Classify the preparation.
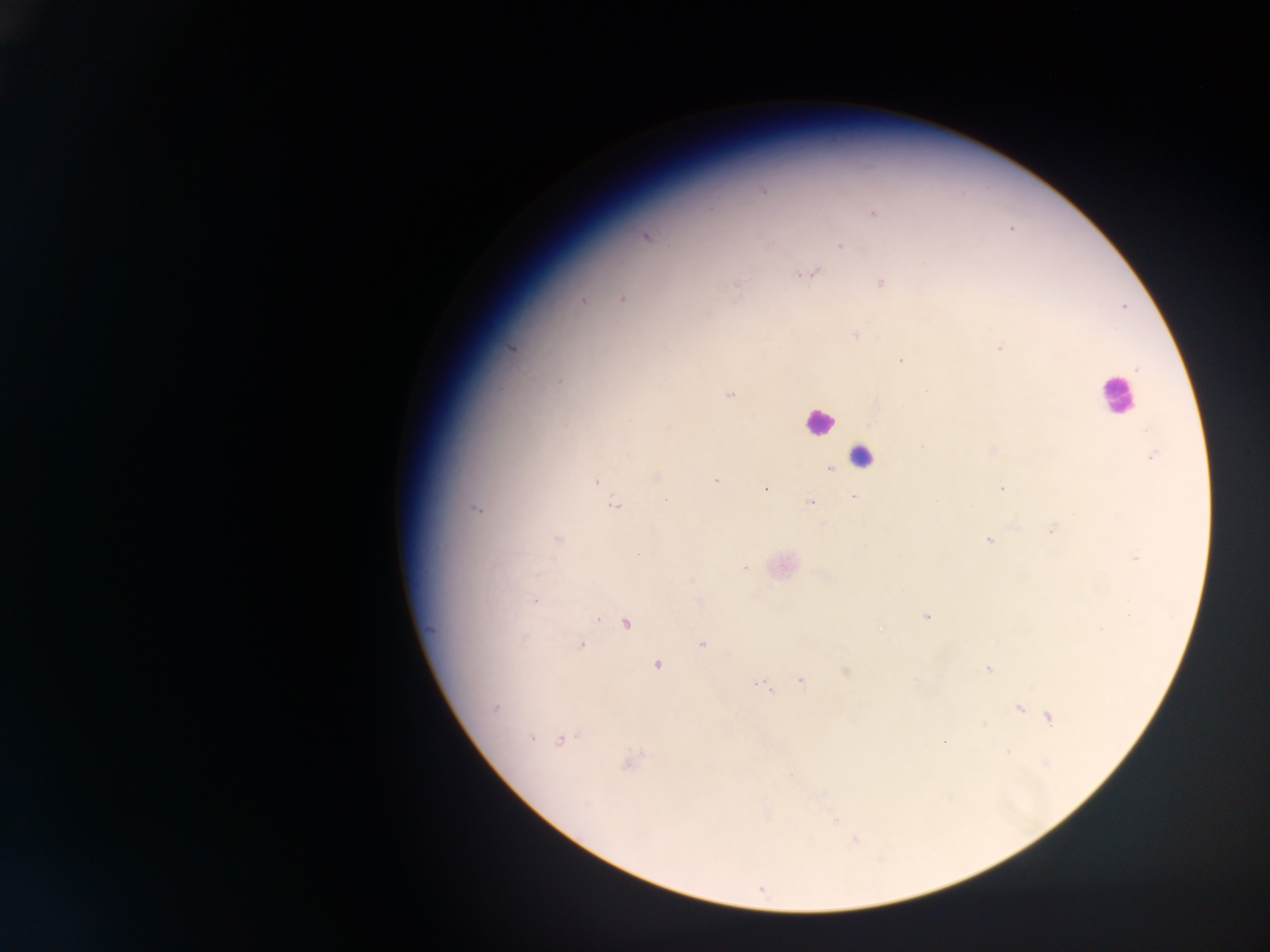

This is a thick smear.

Approximate centers as [x, y] in pixels. Leukocyte locations: [1115, 399], [815, 422], [862, 452]. Plasmodium parasite locations: [765, 192], [871, 213], [1011, 228], [646, 235], [766, 245], [838, 245], [815, 272], [797, 275], [879, 282], [736, 284], [582, 299], [623, 299], [1122, 306], [854, 336], [997, 347], [514, 348], [899, 359], [1137, 369], [559, 380], [728, 392], [923, 446], [992, 451], [1151, 455], [830, 470], [717, 479], [596, 481], [1003, 487], [765, 488], [853, 496], [810, 501], [1049, 529], [559, 539], [989, 540], [1134, 557], [743, 566], [535, 600], [926, 616], [596, 618], [625, 623], [881, 628], [432, 629], [703, 644], [581, 645], [656, 665], [987, 670], [845, 672], [800, 679], [914, 679], [773, 693], [497, 707], [1019, 708], [1048, 718], [982, 724], [532, 740], [560, 740], [945, 742], [1007, 751], [626, 765], [835, 820], [853, 840]. Mobile-phone photograph taken through the microscope. Image is 1270×952 pixels. Single field of view. Sample from Ghana.